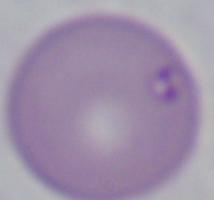
magnification = 1000x
modality = photomicrograph
identification = Babesia